Report the malaria status of this cell.
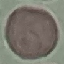

It is uninfected.

Summary:
  - Capture: smartphone camera at the microscope eyepiece
  - Image type: cell patch, automatically extracted from a larger field of view and resized to 64 × 64 pixels
  - Stain: Giemsa
  - Preparation: thin blood smear